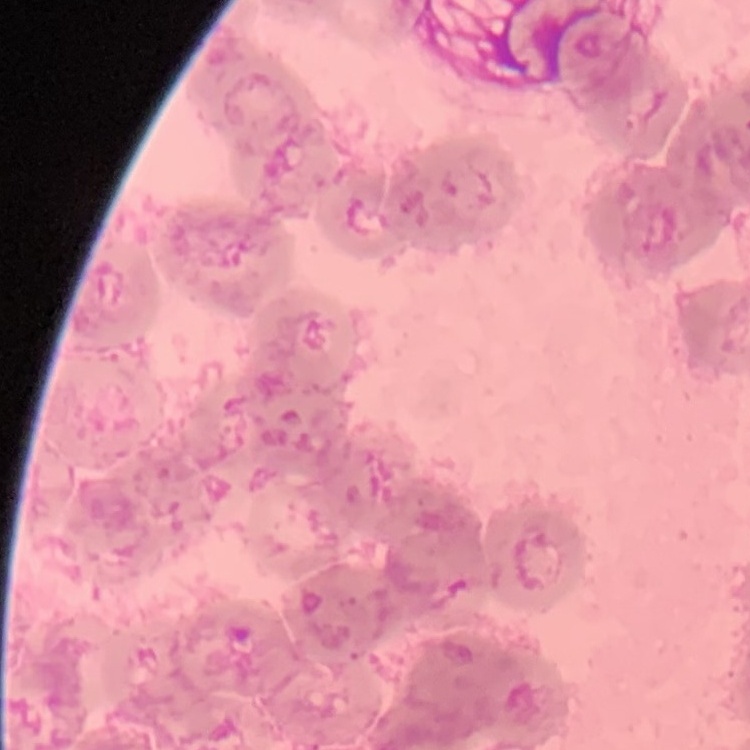
Summary:
  - Red blood cell morphology: rouleaux formation
  - Image type: one tile cut from a larger photomicrograph
  - Stain: Field's or Giemsa
  - Preparation: thin blood smear